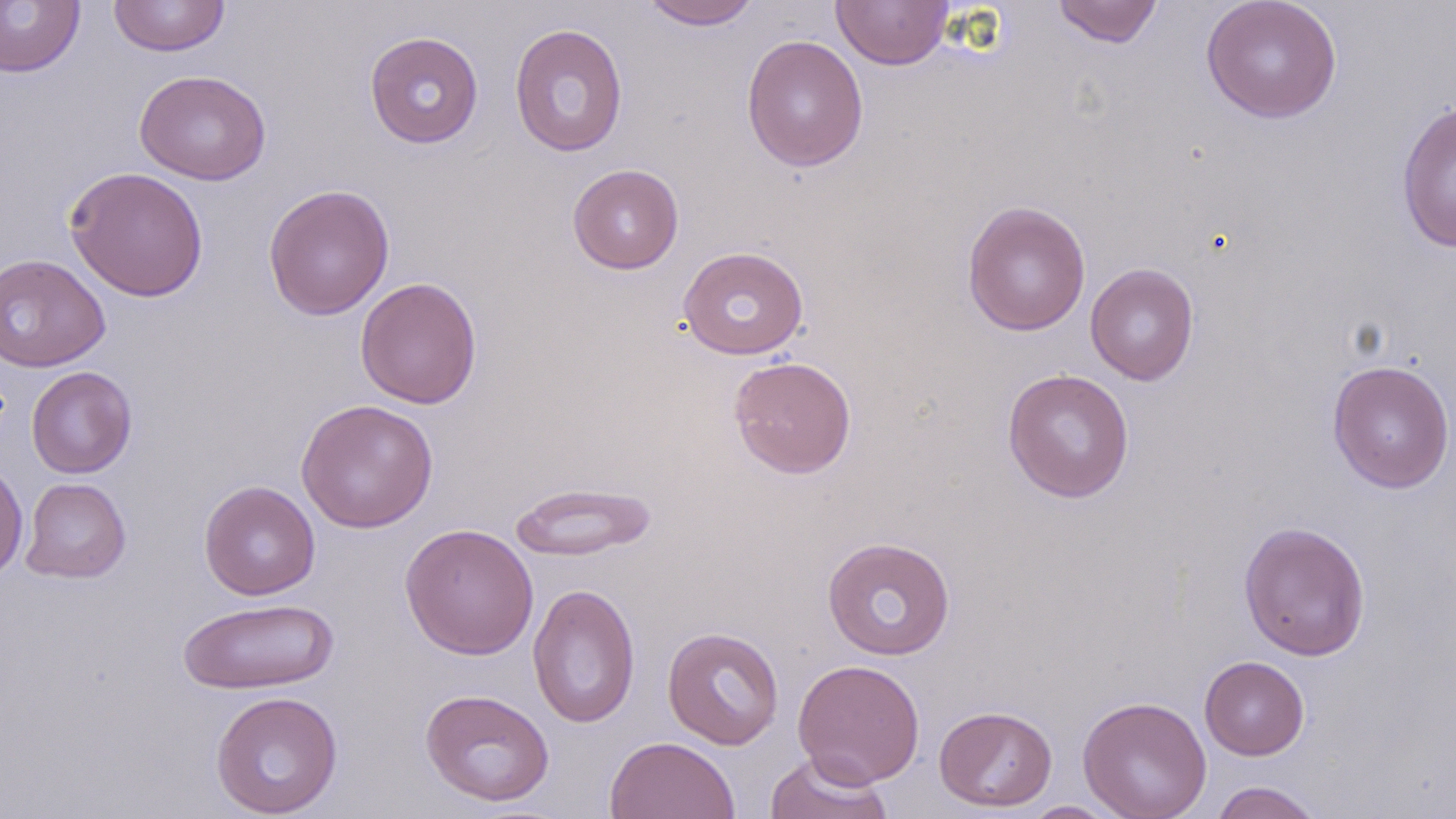
Summary:
  - Coordinate format: approximate bounding boxes as (x1, y1, x2, y2) in pixels
  - Uninfected red blood cell locations: (0, 0, 85, 78), (108, 0, 230, 57), (638, 0, 764, 30), (1051, 0, 1163, 48), (1201, 0, 1342, 123), (831, 1, 953, 70), (509, 23, 629, 157), (364, 31, 484, 148), (741, 34, 869, 173), (134, 69, 272, 186), (1395, 99, 1456, 253), (567, 163, 684, 274), (65, 166, 209, 302), (263, 183, 395, 321), (962, 200, 1091, 337), (678, 246, 809, 360), (0, 253, 110, 372), (1084, 262, 1199, 385), (355, 277, 483, 409), (728, 356, 857, 479), (1327, 359, 1455, 493), (26, 366, 138, 479), (1002, 368, 1135, 503), (296, 398, 439, 533), (0, 460, 28, 582), (21, 477, 131, 583), (199, 480, 320, 600), (509, 481, 657, 562), (1238, 520, 1371, 661), (400, 522, 539, 660), (822, 535, 956, 661), (527, 582, 641, 729), (177, 597, 339, 695), (662, 627, 784, 749), (1199, 656, 1310, 760), (792, 658, 925, 788), (420, 688, 555, 807), (209, 691, 344, 818), (1077, 695, 1212, 819), (934, 705, 1058, 812), (604, 735, 741, 819), (763, 752, 895, 819), (1208, 780, 1326, 819), (1020, 801, 1122, 817)
  - Slide-level diagnosis: negative for blood parasites
  - Field of view: single
  - Stain: May-Grünwald-Giemsa
  - Preparation: thin blood film
  - Image size: 1456×819 pixels
  - Modality: light microscopy
  - Magnification: 1000x